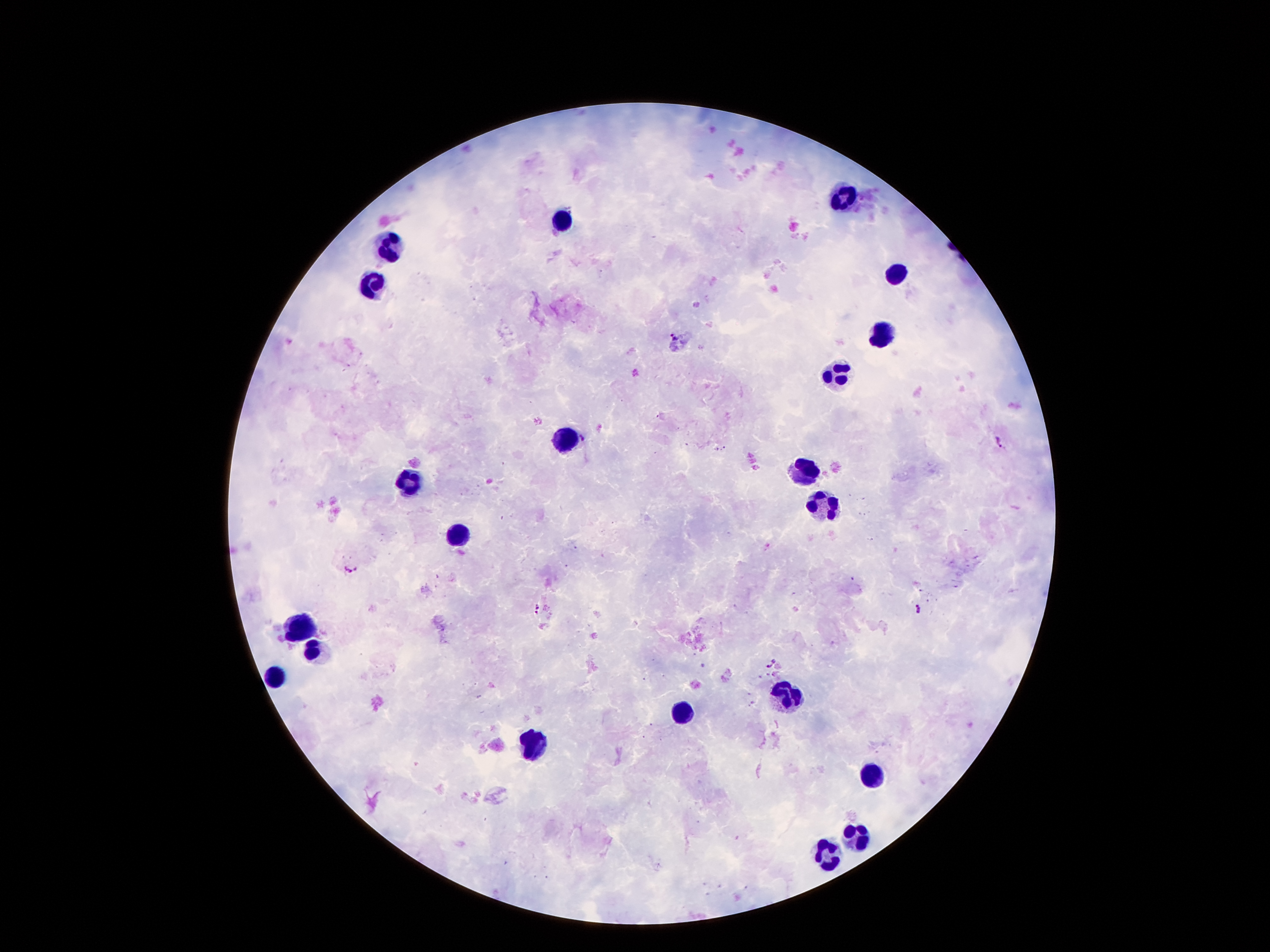
Approximate centers as (x, y) in pixels. Plasmodium parasite locations: (676, 335), (583, 439), (1000, 440), (352, 568), (538, 607), (921, 610), (772, 666). Leukocyte locations: (840, 194), (563, 218), (393, 240), (895, 276), (373, 283), (880, 333), (840, 372), (566, 434), (808, 468), (408, 481), (818, 501), (457, 535), (299, 624), (314, 650), (277, 673), (788, 693), (680, 710), (534, 745), (872, 771), (858, 832), (825, 855). 100x magnification. Image is 1270×952 pixels. Patient malaria status: positive for Plasmodium falciparum. Giemsa stain. Single field of view. Thick peripheral-blood smear. Smartphone photograph taken through the microscope eyepiece.